State which cell type is depicted.
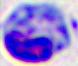

This is a leukocyte.

Photomicrograph. Captured at 400x magnification.